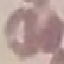

Summary:
  - Malaria status: uninfected
  - Stain: Giemsa
  - Capture: smartphone camera at the microscope eyepiece
  - Preparation: thin smear
  - Image type: automatically extracted cell patch, resized to 64 × 64 pixels